Identify the parasite.
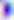
This is Toxoplasma gondii.

Captured at 400x magnification. Micrograph.